Locate every leukocyte (white blood cell).
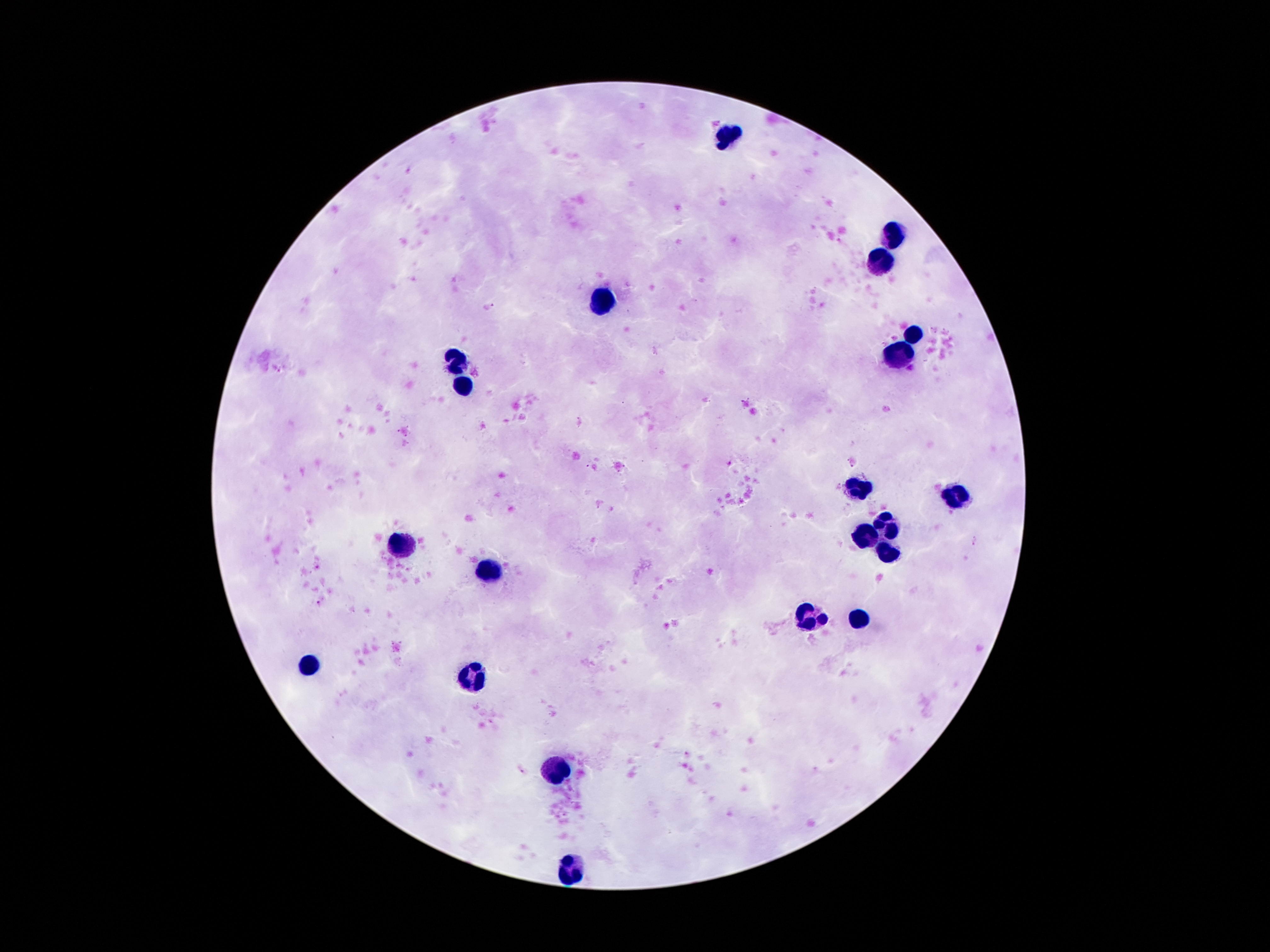
Approximate centers as {x, y} in pixels.
Leukocytes: {728, 137}, {891, 232}, {880, 265}, {603, 298}, {912, 333}, {896, 360}, {452, 363}, {463, 385}, {858, 485}, {958, 495}, {888, 525}, {866, 538}, {403, 544}, {885, 553}, {487, 569}, {809, 618}, {861, 619}, {308, 664}, {471, 677}, {563, 768}, {571, 872}.

Giemsa-stained preparation. Patient malaria status: uninfected. One field from this slide. Thick peripheral-blood smear. Image is 1270×952 pixels. Smartphone photograph taken through the microscope eyepiece. 100x magnification.